Assess this cell for malaria.
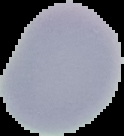
Uninfected.

Image is 124×136 pixels. From a thin blood smear. The area outside the segmented cell region is set to black.